Report the malaria status of this cell.
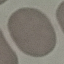
It is uninfected.

Cell patch, automatically extracted from a larger field of view and resized to 64 × 64 pixels. Thin blood film. Giemsa stain. Acquired by smartphone through the microscope eyepiece.